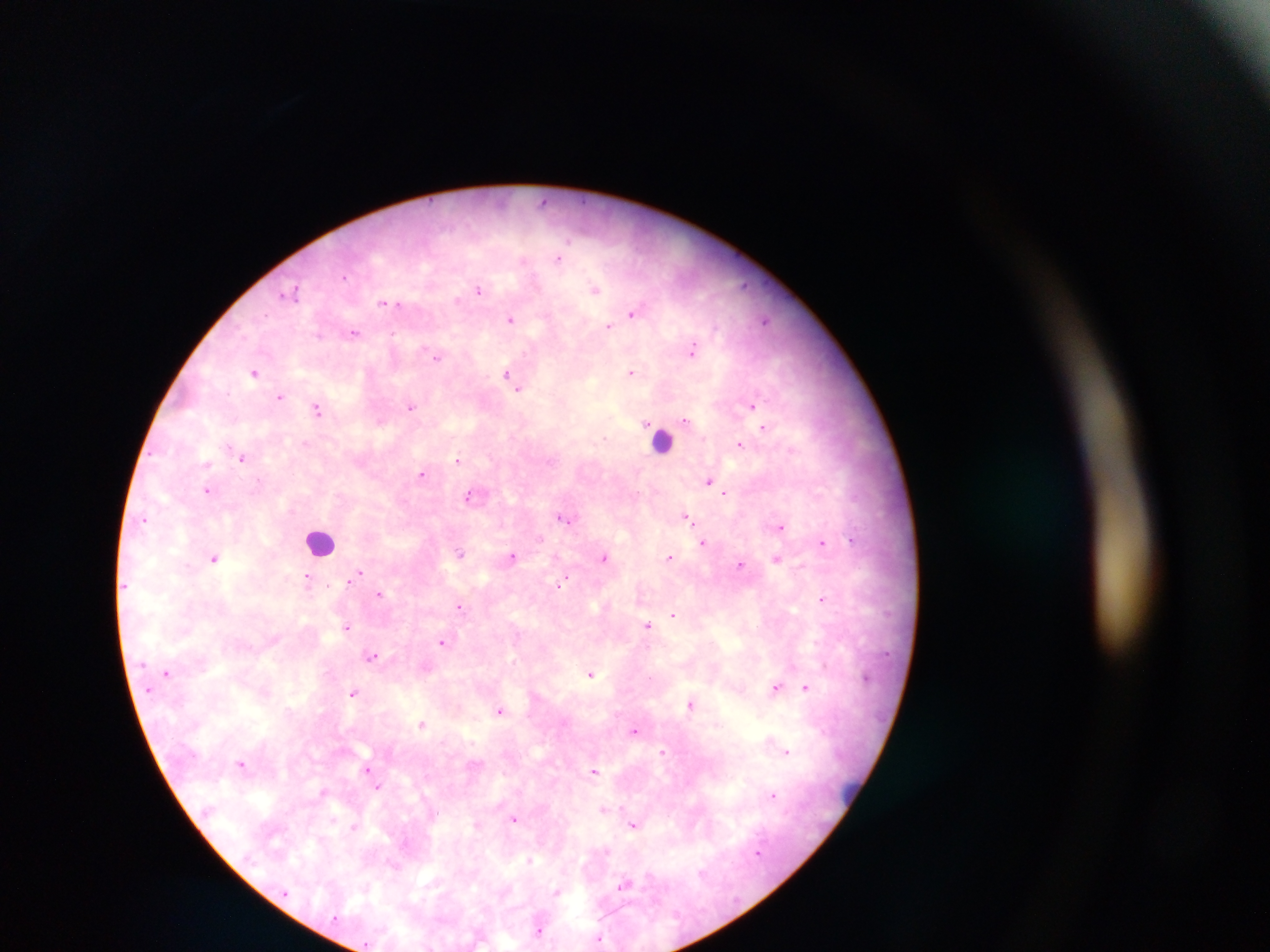
Approximate centers as (x, y) in pixels. Leukocyte locations: (662, 438), (321, 541), (852, 796). Plasmodium parasite locations: (543, 200), (558, 258), (343, 277), (744, 286), (595, 289), (478, 290), (290, 293), (457, 299), (383, 303), (396, 304), (633, 312), (510, 319), (764, 320), (608, 326), (354, 333), (692, 350), (435, 355), (631, 371), (254, 372), (507, 374), (519, 388), (279, 396), (751, 406), (411, 407), (318, 410), (685, 420), (380, 422), (763, 426), (305, 444), (739, 444), (243, 458), (458, 460), (206, 463), (422, 474), (708, 481), (207, 491), (725, 493), (469, 495), (686, 517), (564, 518), (144, 520), (780, 527), (541, 538), (853, 540), (704, 542), (822, 543), (460, 554), (512, 556), (669, 557), (214, 558), (603, 558), (776, 559), (740, 566), (357, 573), (307, 580), (562, 582), (380, 594), (822, 599), (460, 606), (674, 615), (647, 625), (347, 627), (442, 642), (372, 655), (167, 673), (590, 673), (774, 687), (806, 687), (354, 693), (691, 704), (500, 711), (422, 724), (635, 730), (663, 752), (787, 752), (241, 763), (368, 770), (594, 771), (377, 787), (323, 791), (772, 794), (603, 809), (514, 819), (354, 826), (633, 826), (530, 859), (702, 873), (623, 885), (557, 892), (539, 930), (598, 939). Thick blood film. Single field of view. Sample from Ghana. Image is 1270×952 pixels. Mobile-phone photograph taken through the microscope.